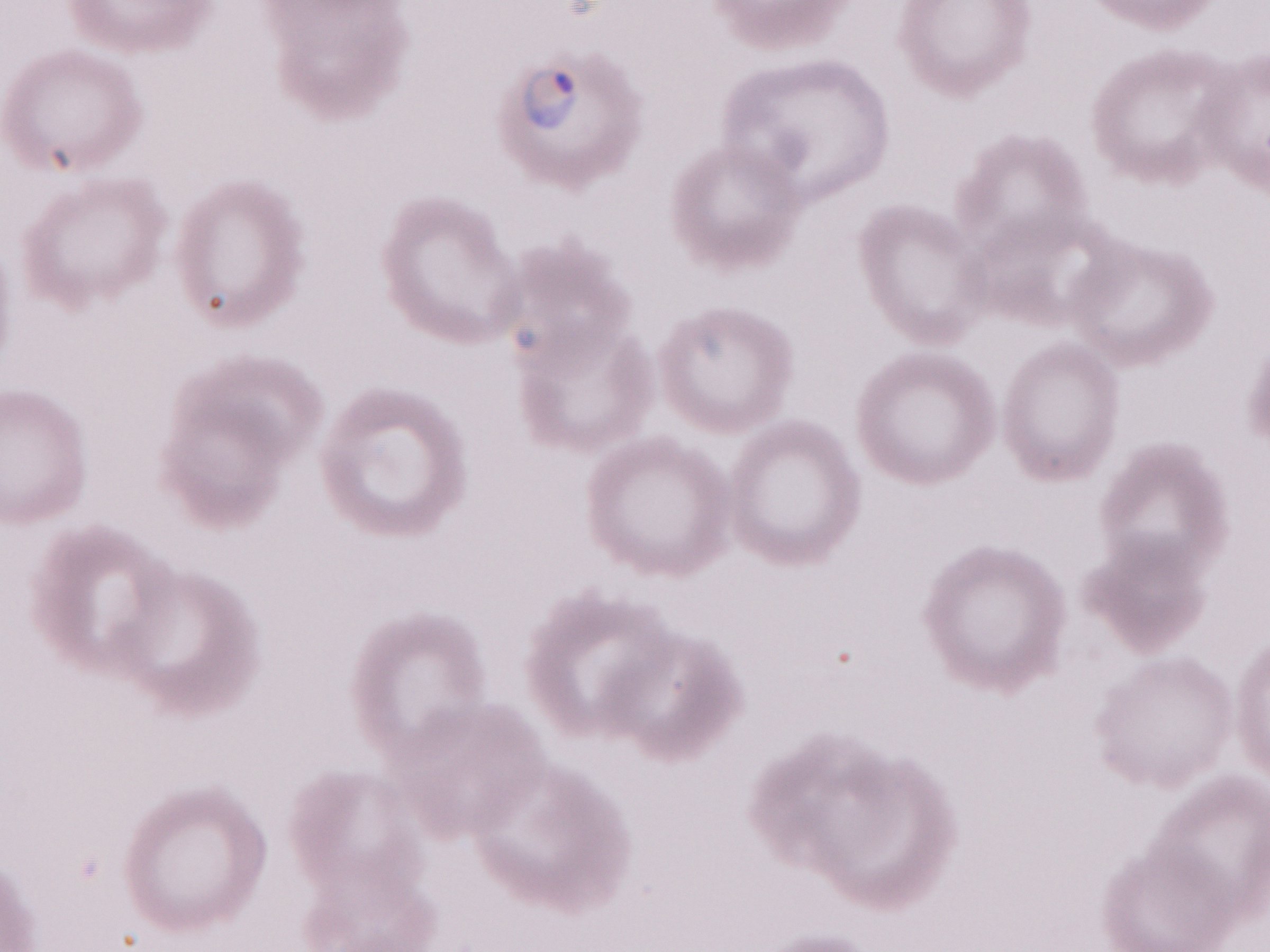
Olympus BX43 microscope and DP73 digital camera. May-Grünwald-Giemsa (MGG) stain. Image is 1270×952 pixels. Single field of view. Thin peripheral-blood smear. 1,000x magnification. Patient-level malaria diagnosis: positive.